Locate every blood parasite and identify its species.
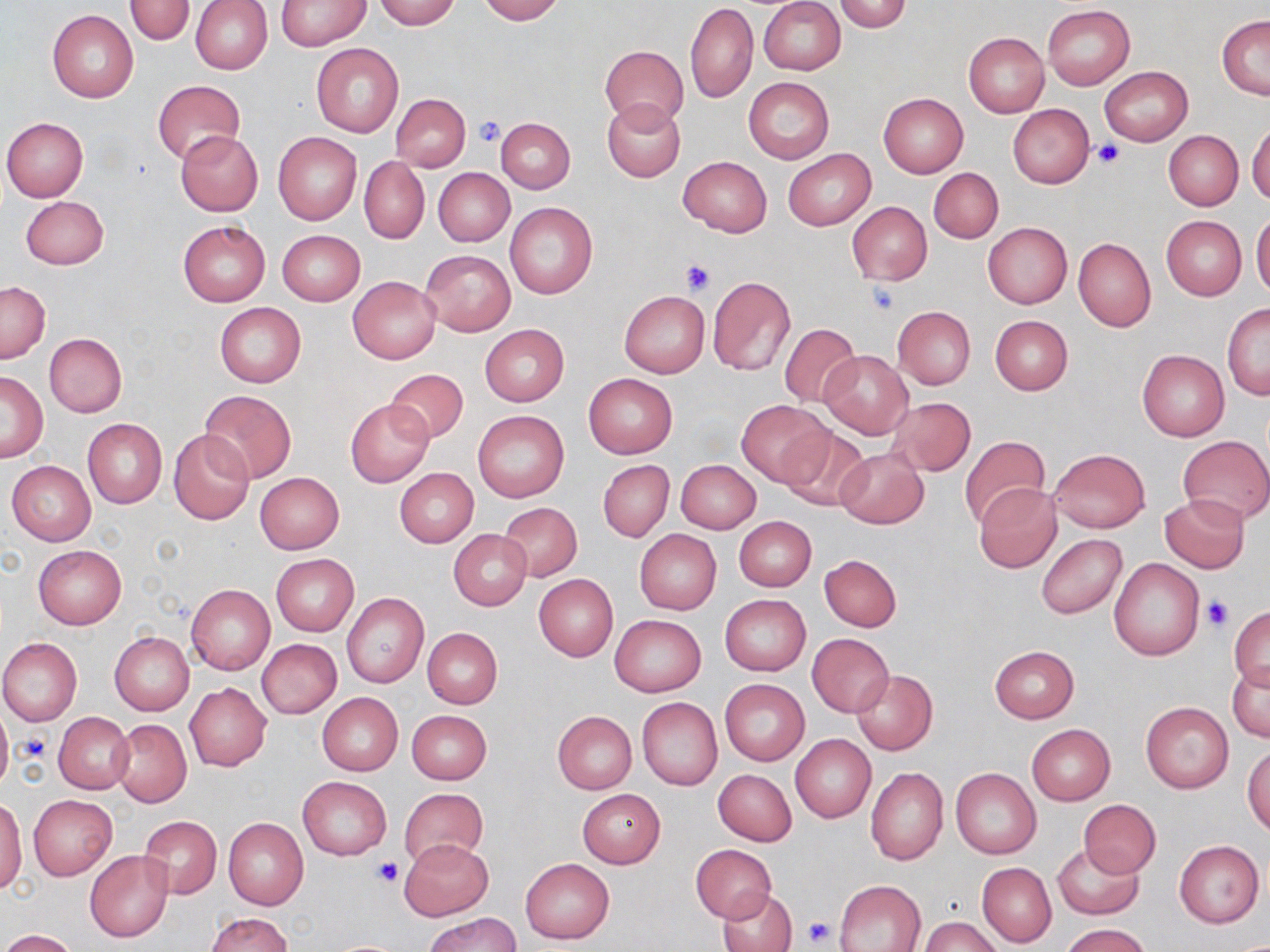

No blood parasites observed.

slide_level_diagnosis: no evidence of blood parasites
uninfected_red_blood_cell_locations: 'approximate bounding boxes as (x1, y1, x2, y2) in pixels: (124, 0, 196, 45), (191, 0, 272, 74), (274, 0, 369, 50), (374, 0, 461, 29), (475, 0, 563, 23), (759, 0, 845, 75), (834, 0, 912, 32), (687, 3, 758, 103), (1042, 5, 1135, 90), (47, 10, 139, 102), (1217, 15, 1270, 99), (963, 32, 1049, 118), (311, 43, 403, 137), (599, 45, 688, 129), (1100, 67, 1193, 145), (743, 77, 835, 164), (152, 80, 244, 166), (391, 93, 471, 172), (878, 93, 968, 178), (602, 99, 686, 182), (1008, 105, 1093, 187), (2, 117, 89, 201), (496, 117, 575, 192), (1247, 124, 1270, 206), (176, 130, 263, 216), (1164, 131, 1243, 210), (273, 132, 362, 225), (784, 150, 874, 230), (678, 156, 771, 236), (360, 157, 428, 243), (432, 167, 514, 247), (928, 167, 1003, 243), (19, 196, 108, 270), (847, 201, 932, 286), (505, 203, 597, 298), (1251, 213, 1270, 298), (1162, 217, 1246, 299), (178, 220, 270, 306), (982, 222, 1073, 309), (277, 229, 365, 306), (1074, 238, 1156, 331), (420, 250, 516, 335), (707, 275, 796, 377), (348, 276, 440, 362), (1, 281, 50, 363), (620, 291, 709, 377), (214, 302, 306, 387), (1222, 304, 1270, 399), (892, 307, 975, 389), (989, 314, 1073, 394), (780, 323, 861, 408), (480, 324, 569, 406), (43, 333, 127, 418), (820, 350, 912, 439), (1137, 350, 1229, 442), (384, 368, 469, 445), (0, 372, 47, 462), (584, 374, 677, 458), (198, 389, 297, 483), (886, 397, 976, 475), (345, 399, 433, 486), (737, 402, 832, 486), (472, 409, 569, 502), (82, 419, 167, 509), (780, 427, 871, 511), (169, 429, 254, 525), (959, 435, 1050, 528), (1179, 435, 1270, 524), (834, 446, 928, 529), (1049, 448, 1150, 533), (7, 460, 96, 546), (598, 460, 674, 541), (676, 460, 760, 534), (394, 468, 478, 547), (254, 472, 344, 553), (975, 484, 1061, 572), (1159, 494, 1249, 574), (498, 502, 582, 581), (734, 515, 817, 591), (448, 529, 531, 610), (634, 529, 721, 613), (1036, 533, 1126, 619), (33, 545, 127, 628), (270, 554, 359, 636), (820, 554, 901, 631), (1109, 557, 1205, 660), (534, 574, 618, 661), (186, 584, 274, 674), (341, 591, 428, 688), (719, 594, 810, 676), (1230, 606, 1270, 688), (609, 614, 706, 696), (422, 627, 503, 708), (109, 631, 194, 714), (806, 633, 894, 716), (0, 638, 82, 726), (257, 639, 342, 719), (989, 645, 1079, 723), (1228, 659, 1269, 742), (852, 669, 937, 755), (719, 679, 810, 765), (185, 683, 271, 771), (316, 693, 403, 774), (636, 697, 722, 790), (1141, 702, 1234, 793), (0, 705, 12, 792), (407, 709, 491, 785), (552, 710, 636, 794), (53, 713, 134, 794), (112, 719, 191, 806), (1025, 724, 1115, 806), (791, 735, 875, 823), (1244, 746, 1270, 836), (866, 767, 948, 865), (951, 768, 1041, 859), (713, 769, 797, 846), (297, 776, 392, 860), (400, 787, 489, 870), (577, 789, 666, 867), (28, 795, 117, 879), (0, 796, 27, 895), (1079, 799, 1161, 878), (140, 816, 222, 897), (223, 818, 308, 910), (399, 840, 493, 920), (1175, 841, 1264, 927), (1052, 843, 1145, 920), (689, 844, 777, 923), (85, 849, 173, 942), (521, 858, 614, 944), (977, 863, 1055, 946), (835, 880, 926, 951), (719, 887, 797, 952), (207, 912, 292, 951), (427, 914, 521, 952), (920, 916, 1001, 952), (1062, 922, 1151, 952), (2, 929, 77, 952)'
modality: light microscopy
field_of_view: one of a larger specimen
platelet_locations: 'approximate bounding boxes as (x1, y1, x2, y2) in pixels: (473, 115, 507, 146), (1094, 140, 1124, 168), (680, 261, 714, 295), (868, 281, 900, 314), (1203, 596, 1234, 631), (20, 732, 51, 762), (372, 857, 401, 886), (803, 916, 836, 948)'
image_size: 1270×952 pixels
magnification: 1000x
preparation: thin blood film
stain: May-Grünwald-Giemsa